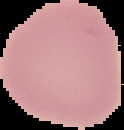
image type = segmented cell region with the area outside set to black
malaria status = uninfected
image size = 124×130 pixels
preparation = thin blood film